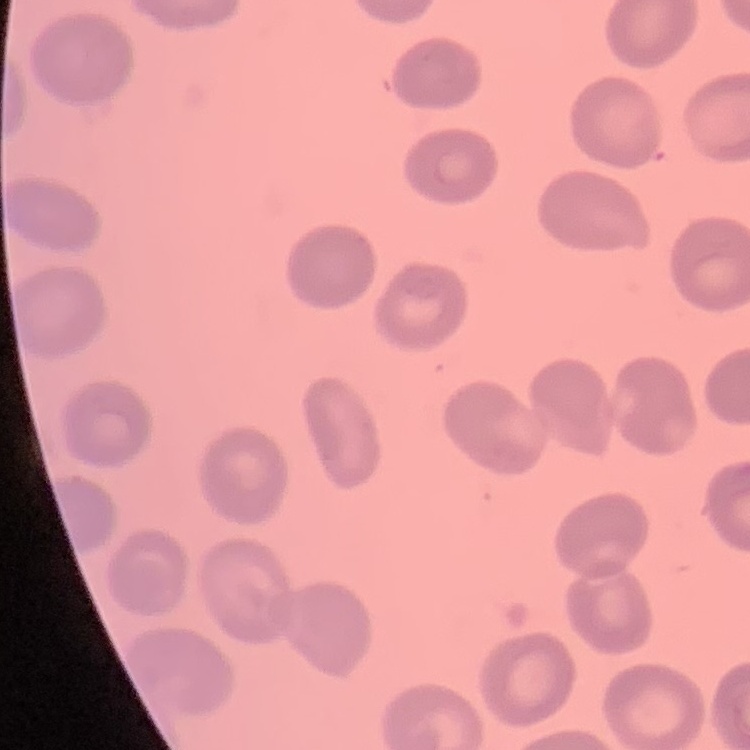

Summary:
  - Red blood cell morphology: no rouleaux formation
  - Stain: Field's or Giemsa
  - Image type: square crop of a larger photomicrograph
  - Preparation: thin peripheral smear